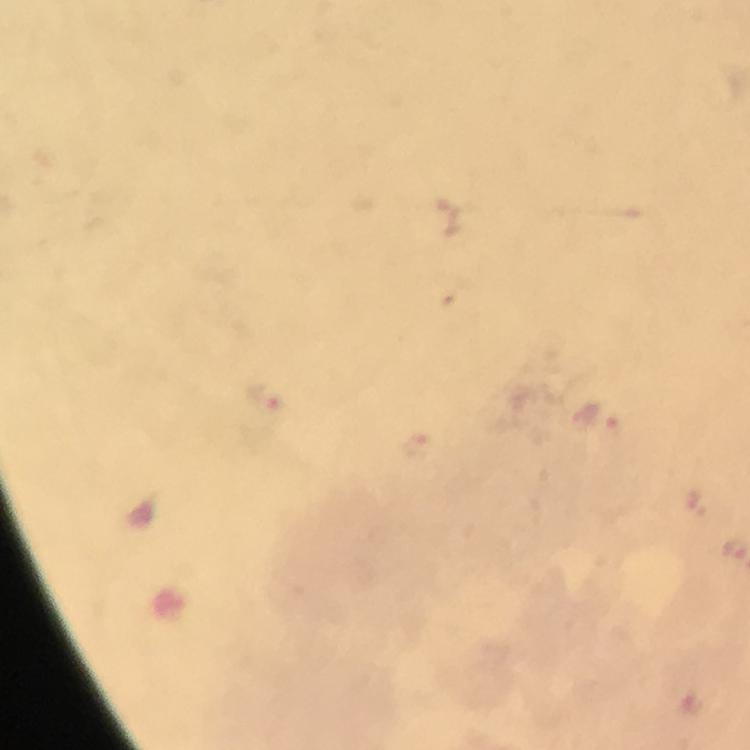
cropped from = a single field of view
image size = 750×750 pixels
capture = smartphone camera through the microscope
preparation = thick blood film
context = from a diagnostic examination for malaria
magnification = 100x
Plasmodium parasite locations = approximate centers as (x, y) in pixels: (267, 396), (595, 418), (693, 500)
stain = Giemsa
immersion oil = applied